State the blood parasite species.
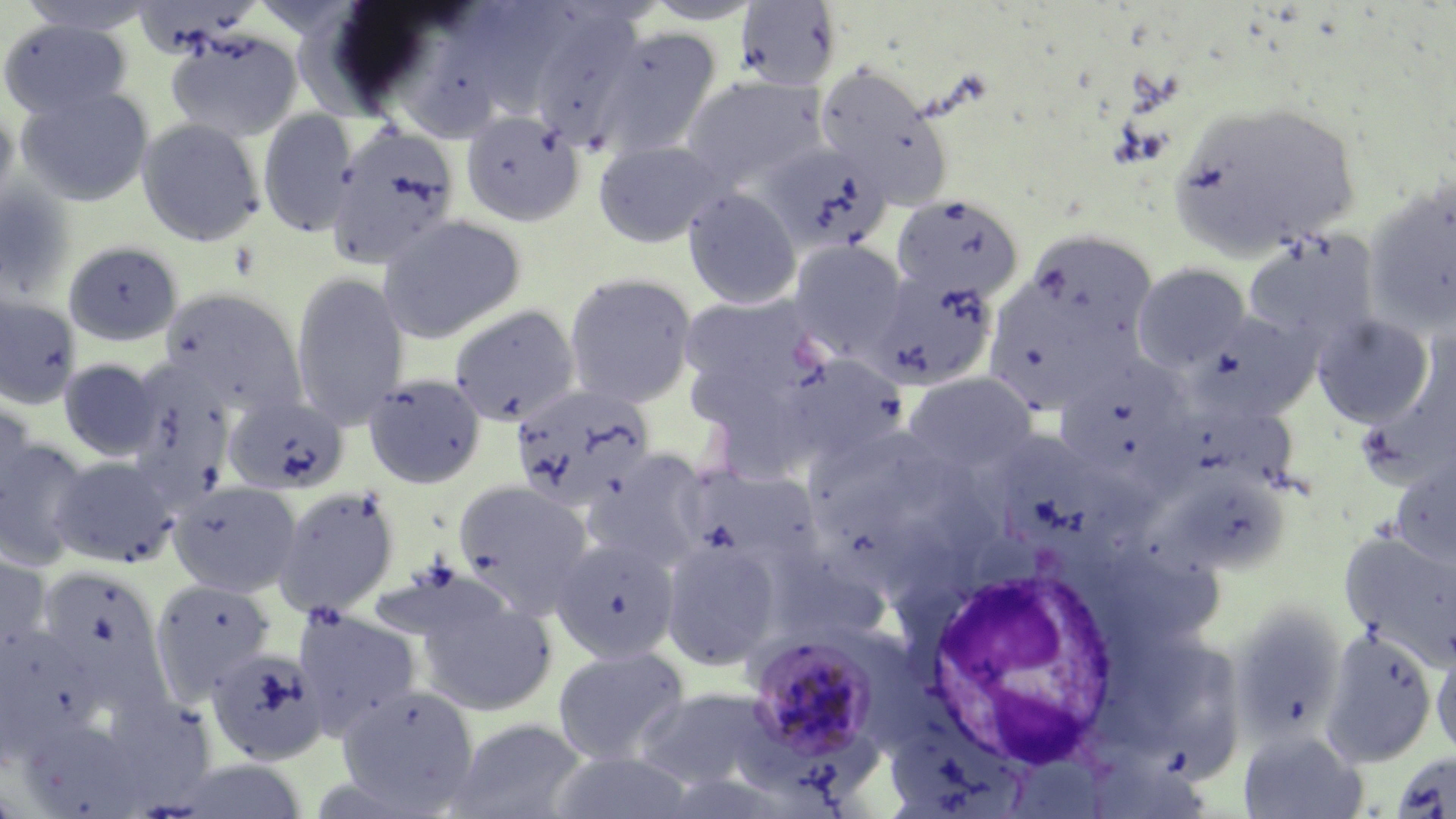
Plasmodium malariae.

modality = light microscopy
uninfected red blood cell locations = approximate bounding boxes as [x1, y1, x2, y2] in pixels: [16, 0, 161, 34], [641, 1, 764, 25], [735, 1, 843, 90], [517, 4, 650, 145], [382, 5, 517, 143], [0, 17, 132, 120], [590, 24, 723, 158], [166, 29, 302, 142], [815, 65, 954, 210], [682, 75, 825, 189], [17, 87, 154, 206], [1166, 99, 1364, 259], [0, 104, 19, 223], [258, 109, 358, 237], [460, 110, 584, 227], [137, 118, 265, 246], [326, 124, 462, 269], [593, 140, 726, 248], [759, 143, 891, 256], [1364, 178, 1456, 337], [1, 183, 75, 303], [683, 188, 802, 309], [891, 192, 1026, 304], [376, 214, 527, 343], [1026, 229, 1156, 347], [1242, 231, 1378, 351], [788, 239, 908, 360], [64, 240, 183, 347], [1132, 263, 1250, 372], [867, 268, 1000, 391], [291, 271, 408, 429], [563, 272, 698, 408], [982, 276, 1134, 414], [161, 286, 307, 414], [678, 292, 823, 408], [0, 296, 82, 409], [449, 303, 581, 427], [1198, 311, 1320, 421], [1313, 314, 1434, 428], [777, 352, 911, 469], [1052, 353, 1197, 489], [58, 358, 161, 460], [125, 359, 239, 493], [903, 371, 1037, 478], [363, 372, 487, 488], [509, 383, 655, 511], [223, 395, 349, 495], [0, 398, 39, 512], [1003, 431, 1126, 557], [0, 435, 92, 571], [581, 448, 713, 574], [1390, 452, 1456, 570], [48, 454, 179, 569], [50, 461, 300, 582], [681, 464, 826, 581], [1157, 467, 1290, 576], [452, 478, 594, 611], [167, 480, 302, 598], [272, 485, 401, 616], [823, 509, 967, 608], [1340, 530, 1456, 673], [660, 534, 783, 671], [549, 536, 680, 664], [0, 552, 52, 672], [770, 553, 891, 647], [34, 564, 165, 693], [150, 578, 277, 702], [414, 591, 559, 719], [1230, 602, 1347, 743], [293, 605, 422, 740], [0, 626, 98, 759], [1320, 628, 1438, 767], [1156, 640, 1252, 781], [1433, 641, 1456, 767], [206, 645, 331, 765], [551, 645, 691, 765], [336, 684, 480, 811], [633, 687, 782, 793], [446, 717, 590, 819], [19, 718, 149, 819], [1238, 729, 1368, 819], [547, 749, 699, 819], [1391, 752, 1456, 819], [166, 758, 311, 817]
image size = 1456×819 pixels
white blood cell locations = approximate bounding boxes as [x1, y1, x2, y2] in pixels: [918, 560, 1123, 771]
preparation = thin blood smear
magnification = 1000x
field of view = one of a larger specimen
stain = May-Grünwald-Giemsa
Plasmodium malariae-infected red blood cell locations = approximate bounding boxes as [x1, y1, x2, y2] in pixels: [744, 633, 880, 770]